Report the malaria status of this cell.
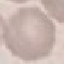

It is uninfected.

Summary:
  - Stain: Giemsa
  - Capture: smartphone through the microscope eyepiece
  - Image type: cell patch, automatically extracted from a larger field of view and resized to 64 × 64 pixels
  - Preparation: thin blood smear